Find each cell and give its type.
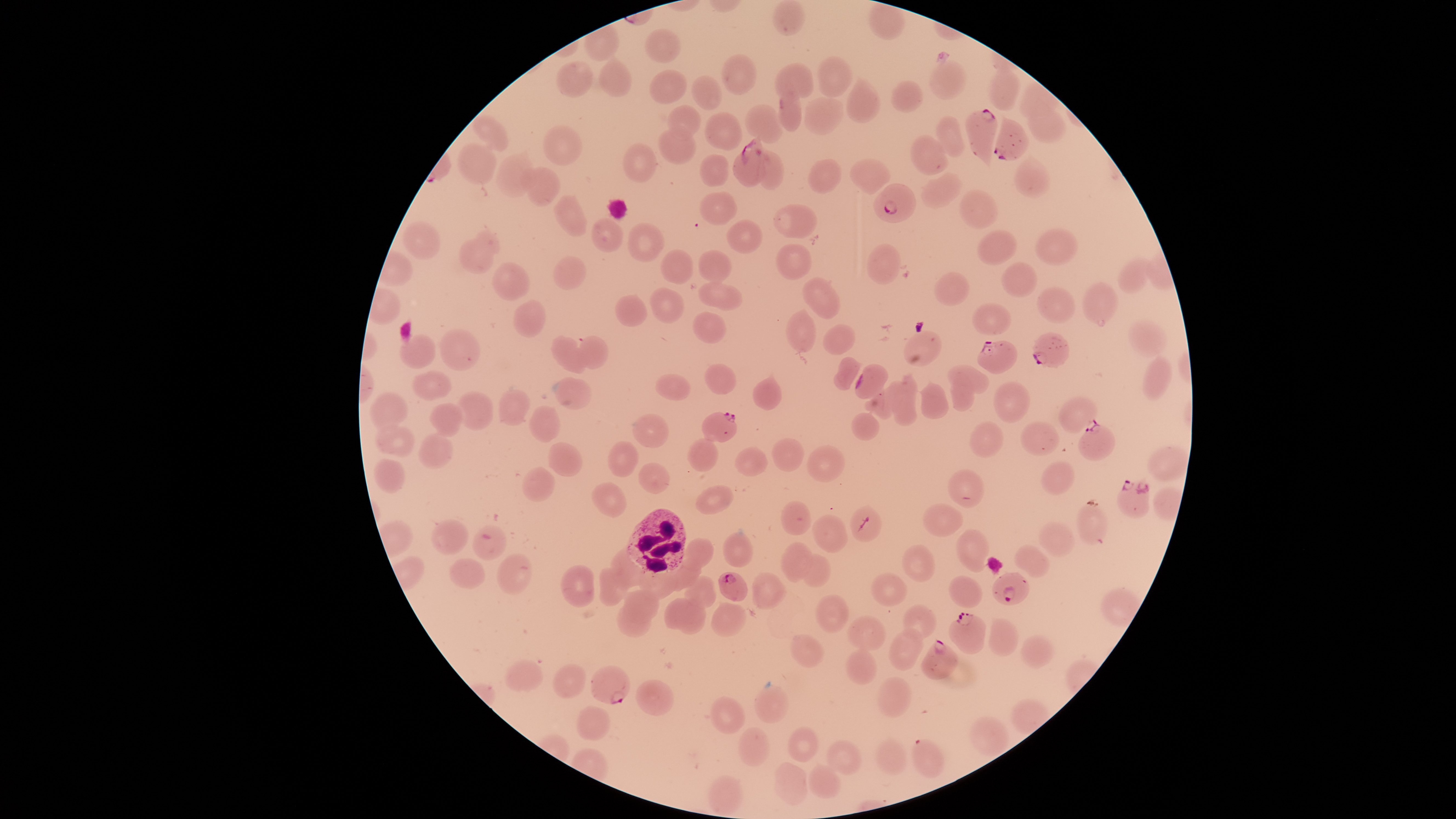

Approximate bounding boxes, in pixels from the top-left corner.
Parasitized red blood cells: (left=963, top=107, right=999, bottom=172), (left=993, top=114, right=1030, bottom=162), (left=731, top=133, right=769, bottom=187), (left=873, top=183, right=917, bottom=223), (left=1032, top=331, right=1070, bottom=369), (left=977, top=339, right=1018, bottom=375), (left=854, top=363, right=889, bottom=399), (left=701, top=411, right=738, bottom=443), (left=1077, top=420, right=1117, bottom=461), (left=1116, top=477, right=1150, bottom=519), (left=849, top=504, right=882, bottom=542), (left=472, top=524, right=507, bottom=561), (left=719, top=571, right=749, bottom=602), (left=991, top=571, right=1030, bottom=605), (left=947, top=611, right=987, bottom=655), (left=920, top=636, right=960, bottom=680), (left=589, top=664, right=631, bottom=704), (left=910, top=738, right=945, bottom=779).
Uninfected red blood cells: (left=771, top=0, right=806, bottom=37), (left=868, top=1, right=905, bottom=40), (left=644, top=28, right=681, bottom=63), (left=597, top=54, right=632, bottom=98), (left=720, top=54, right=758, bottom=95), (left=817, top=55, right=854, bottom=98), (left=928, top=59, right=967, bottom=100), (left=988, top=59, right=1020, bottom=111), (left=555, top=60, right=594, bottom=97), (left=773, top=63, right=814, bottom=110), (left=649, top=69, right=687, bottom=105), (left=691, top=74, right=722, bottom=110), (left=845, top=74, right=882, bottom=123), (left=889, top=79, right=925, bottom=113), (left=1019, top=81, right=1061, bottom=120), (left=778, top=88, right=802, bottom=133), (left=1027, top=94, right=1066, bottom=144), (left=803, top=96, right=844, bottom=135), (left=667, top=103, right=701, bottom=140), (left=744, top=104, right=785, bottom=144), (left=703, top=111, right=742, bottom=151), (left=471, top=115, right=509, bottom=151), (left=934, top=115, right=966, bottom=157), (left=542, top=124, right=584, bottom=166), (left=657, top=126, right=696, bottom=164), (left=910, top=134, right=949, bottom=175), (left=456, top=140, right=497, bottom=185), (left=621, top=142, right=658, bottom=183), (left=494, top=147, right=536, bottom=199), (left=760, top=149, right=785, bottom=190), (left=698, top=152, right=730, bottom=187), (left=1014, top=154, right=1051, bottom=198), (left=848, top=157, right=892, bottom=195), (left=807, top=158, right=842, bottom=194), (left=519, top=166, right=561, bottom=208), (left=920, top=171, right=963, bottom=209), (left=958, top=188, right=999, bottom=230), (left=698, top=191, right=737, bottom=225), (left=553, top=194, right=588, bottom=236), (left=772, top=203, right=818, bottom=239), (left=591, top=217, right=623, bottom=252), (left=727, top=219, right=764, bottom=254), (left=401, top=220, right=441, bottom=260), (left=626, top=222, right=665, bottom=262), (left=1034, top=227, right=1078, bottom=266), (left=458, top=228, right=501, bottom=276), (left=977, top=229, right=1018, bottom=265), (left=775, top=243, right=812, bottom=281), (left=866, top=243, right=901, bottom=286), (left=659, top=249, right=694, bottom=285), (left=697, top=249, right=733, bottom=284), (left=1118, top=255, right=1155, bottom=294), (left=552, top=256, right=586, bottom=290), (left=490, top=261, right=531, bottom=301), (left=1000, top=261, right=1039, bottom=298), (left=933, top=271, right=970, bottom=306), (left=801, top=276, right=841, bottom=320), (left=1081, top=280, right=1120, bottom=327), (left=698, top=282, right=743, bottom=311), (left=649, top=286, right=685, bottom=323), (left=1035, top=286, right=1076, bottom=324), (left=614, top=293, right=647, bottom=327), (left=513, top=300, right=547, bottom=338), (left=972, top=302, right=1012, bottom=334), (left=786, top=308, right=817, bottom=353), (left=692, top=311, right=727, bottom=344), (left=1127, top=317, right=1169, bottom=358), (left=822, top=323, right=856, bottom=355), (left=439, top=329, right=481, bottom=371), (left=903, top=329, right=942, bottom=368), (left=399, top=333, right=436, bottom=369), (left=549, top=334, right=586, bottom=374), (left=577, top=335, right=610, bottom=369), (left=1141, top=353, right=1172, bottom=402), (left=833, top=355, right=864, bottom=391), (left=703, top=363, right=737, bottom=394), (left=946, top=363, right=990, bottom=393), (left=410, top=370, right=451, bottom=401), (left=753, top=370, right=783, bottom=411), (left=654, top=373, right=691, bottom=401), (left=888, top=373, right=919, bottom=427), (left=551, top=376, right=592, bottom=410), (left=950, top=377, right=975, bottom=413), (left=918, top=380, right=950, bottom=420), (left=992, top=380, right=1030, bottom=424), (left=863, top=383, right=901, bottom=419), (left=497, top=388, right=531, bottom=427), (left=457, top=389, right=494, bottom=431), (left=369, top=390, right=409, bottom=434), (left=1057, top=395, right=1098, bottom=434), (left=429, top=403, right=463, bottom=438), (left=528, top=405, right=561, bottom=444), (left=631, top=412, right=669, bottom=449), (left=850, top=412, right=880, bottom=442), (left=969, top=420, right=1004, bottom=457), (left=1019, top=420, right=1061, bottom=457), (left=376, top=423, right=416, bottom=459), (left=418, top=431, right=454, bottom=470), (left=686, top=437, right=719, bottom=472), (left=770, top=437, right=805, bottom=472), (left=607, top=439, right=640, bottom=477), (left=548, top=441, right=583, bottom=478), (left=805, top=443, right=846, bottom=483), (left=733, top=445, right=769, bottom=477), (left=373, top=459, right=406, bottom=494), (left=1040, top=460, right=1075, bottom=495), (left=638, top=462, right=670, bottom=494), (left=522, top=466, right=555, bottom=503), (left=946, top=469, right=986, bottom=509), (left=590, top=481, right=627, bottom=518), (left=694, top=484, right=734, bottom=514), (left=780, top=500, right=812, bottom=536), (left=923, top=502, right=964, bottom=539), (left=1077, top=504, right=1109, bottom=546), (left=811, top=514, right=848, bottom=553), (left=431, top=518, right=469, bottom=555), (left=1037, top=521, right=1076, bottom=557), (left=955, top=528, right=990, bottom=572), (left=723, top=530, right=754, bottom=567), (left=684, top=537, right=715, bottom=574), (left=780, top=540, right=814, bottom=583), (left=901, top=543, right=936, bottom=583), (left=1013, top=544, right=1051, bottom=578), (left=609, top=546, right=639, bottom=584), (left=497, top=552, right=533, bottom=595), (left=799, top=553, right=831, bottom=588), (left=664, top=556, right=702, bottom=592), (left=448, top=558, right=486, bottom=589), (left=560, top=564, right=595, bottom=608), (left=598, top=566, right=628, bottom=606), (left=751, top=572, right=787, bottom=609), (left=871, top=572, right=907, bottom=607), (left=637, top=573, right=679, bottom=600), (left=684, top=574, right=717, bottom=608), (left=948, top=575, right=984, bottom=608), (left=623, top=588, right=660, bottom=624), (left=815, top=594, right=849, bottom=633), (left=664, top=597, right=693, bottom=630), (left=677, top=599, right=707, bottom=635), (left=615, top=602, right=652, bottom=638), (left=709, top=602, right=747, bottom=638), (left=902, top=603, right=937, bottom=640), (left=846, top=615, right=887, bottom=651), (left=987, top=617, right=1020, bottom=657), (left=888, top=627, right=924, bottom=671), (left=789, top=633, right=825, bottom=667), (left=1019, top=635, right=1055, bottom=669), (left=845, top=643, right=877, bottom=685), (left=505, top=657, right=544, bottom=691), (left=552, top=663, right=586, bottom=698), (left=875, top=676, right=912, bottom=719), (left=635, top=677, right=675, bottom=715), (left=753, top=686, right=791, bottom=724), (left=709, top=695, right=746, bottom=734), (left=575, top=705, right=611, bottom=741), (left=968, top=716, right=1010, bottom=758), (left=737, top=725, right=771, bottom=767), (left=785, top=726, right=819, bottom=762), (left=873, top=737, right=907, bottom=775), (left=824, top=739, right=862, bottom=776), (left=774, top=762, right=809, bottom=805), (left=808, top=763, right=841, bottom=799), (left=708, top=775, right=744, bottom=816).
White blood cells: (left=625, top=508, right=686, bottom=577).

preparation = thin smear of blood
capture = smartphone photograph through the microscope eyepiece
visible region = circular
field of view = single
species = Plasmodium falciparum
stain = Giemsa
image size = 1456×819 pixels